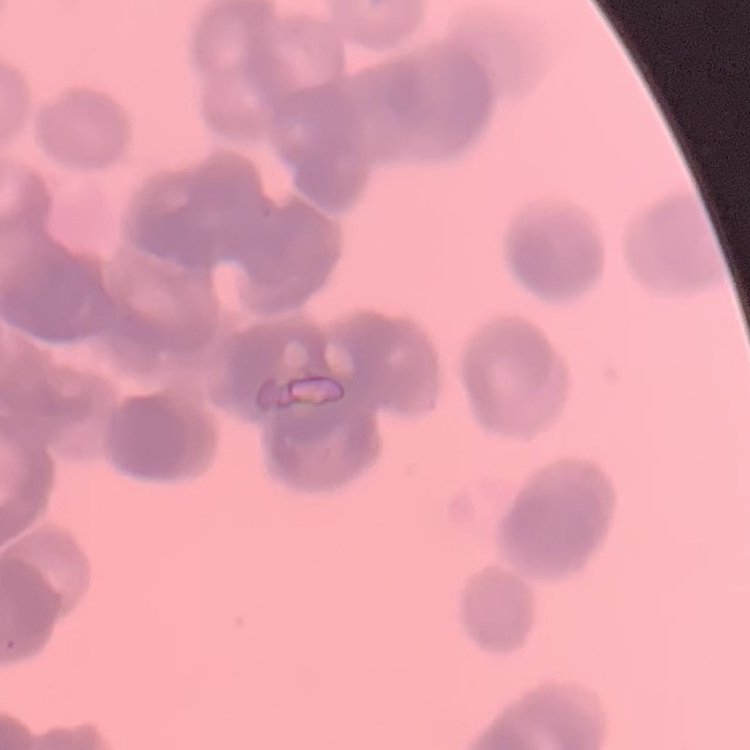
erythrocyte_morphology: rouleaux formation
image_type: one tile cut from a larger photomicrograph
preparation: thin peripheral smear
stain: Field's or Giemsa